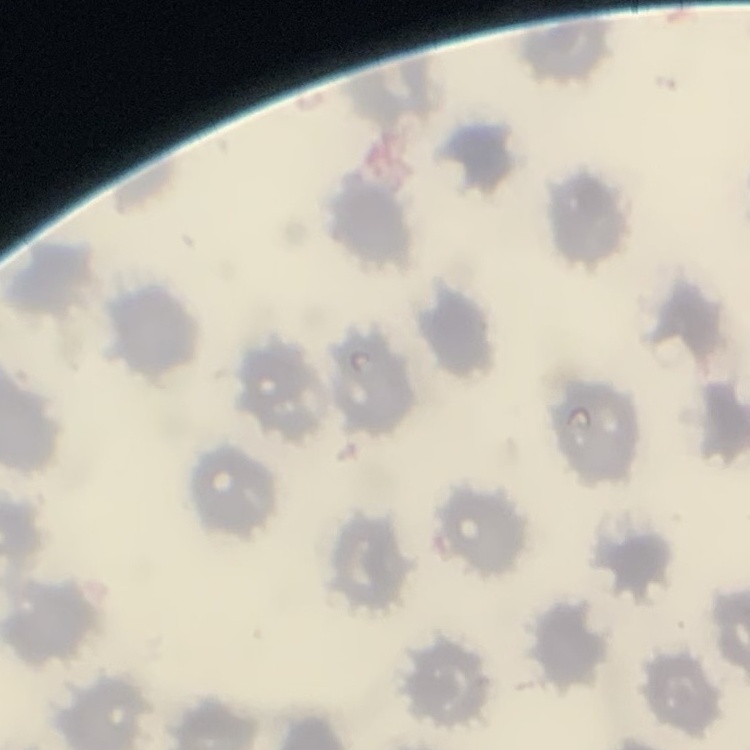 The erythrocytes exhibit no rouleaux formation. Field's or Giemsa stain. Thin peripheral smear. One tile cut from a larger photomicrograph.